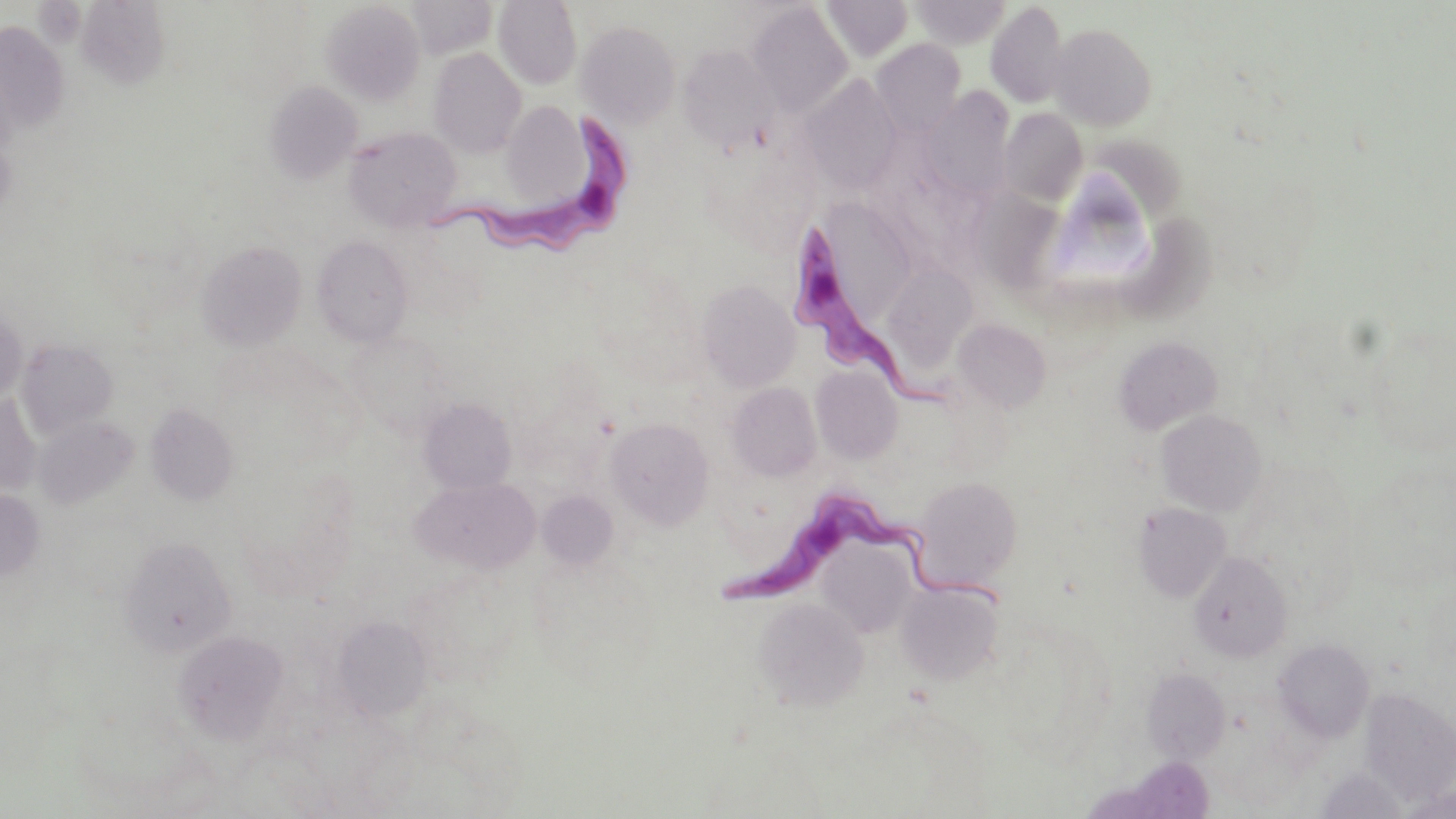

{
  "slide_level_diagnosis": "Trypanosoma brucei",
  "image_size": "1456×819 pixels",
  "modality": "optical microscopy",
  "uninfected_red_blood_cell_locations": "approximate bounding boxes as (x1, y1, x2, y2) in pixels: (407, 0, 497, 58), (493, 0, 581, 90), (821, 1, 914, 60), (910, 1, 1011, 48), (320, 2, 426, 106), (985, 2, 1069, 108), (747, 3, 854, 118), (576, 20, 681, 127), (0, 22, 68, 133), (1049, 23, 1157, 130), (871, 39, 966, 137), (677, 46, 780, 153), (429, 47, 527, 157), (798, 76, 901, 189), (262, 81, 362, 183), (922, 87, 1014, 200), (501, 101, 592, 208), (999, 109, 1087, 206), (343, 127, 461, 231), (1090, 140, 1193, 229), (964, 188, 1062, 292), (822, 198, 910, 321), (1119, 214, 1221, 325), (313, 235, 413, 346), (195, 239, 306, 351), (889, 263, 980, 376), (697, 280, 800, 391), (0, 308, 26, 408), (953, 319, 1052, 412), (1112, 336, 1222, 435), (18, 337, 117, 438), (811, 366, 903, 463), (728, 382, 821, 481), (0, 392, 41, 495), (419, 398, 516, 494), (146, 404, 238, 504), (1156, 409, 1267, 516), (33, 416, 140, 510), (604, 417, 714, 529), (412, 476, 539, 572), (912, 476, 1022, 589), (0, 488, 45, 584), (540, 488, 625, 572), (1133, 503, 1232, 602), (118, 535, 236, 657), (822, 545, 921, 633), (1188, 551, 1293, 662), (897, 582, 1003, 685), (753, 597, 868, 709), (334, 615, 433, 720), (172, 630, 289, 743), (1273, 639, 1374, 742), (1141, 667, 1231, 763), (1361, 690, 1456, 803), (450, 717, 528, 793), (1314, 767, 1409, 818), (1398, 781, 1455, 819)",
  "preparation": "thin blood smear",
  "magnification": "1000x",
  "field_of_view": "one of a larger specimen",
  "trypanosoma_brucei_locations": "approximate bounding boxes as (x1, y1, x2, y2) in pixels: (428, 111, 634, 253), (783, 220, 942, 418), (719, 484, 1008, 619)",
  "stain": "May-Grünwald-Giemsa"
}